Assess this cell for malaria.
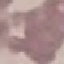
Uninfected.

Summary:
  - Preparation: thin blood smear
  - Capture: smartphone through the microscope eyepiece
  - Image type: cell patch, automatically extracted from a larger field of view and resized to 64 × 64 pixels
  - Stain: Giemsa